Assess this cell for malaria.
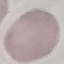

Uninfected.

capture = smartphone through the microscope eyepiece
image type = automatically extracted cell patch, resized to 64 × 64 pixels
stain = Giemsa
preparation = thin smear